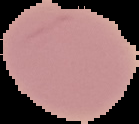
From a thin blood smear. Segmented cell region on a black background. Image is 139×124 pixels. Malaria status: uninfected.